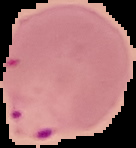 From a thin blood film. Cell region segmented out of the field of view; the surrounding area is masked to black. Image is 136×148 pixels. Result: Plasmodium parasites identified.